Name the blood parasite species.
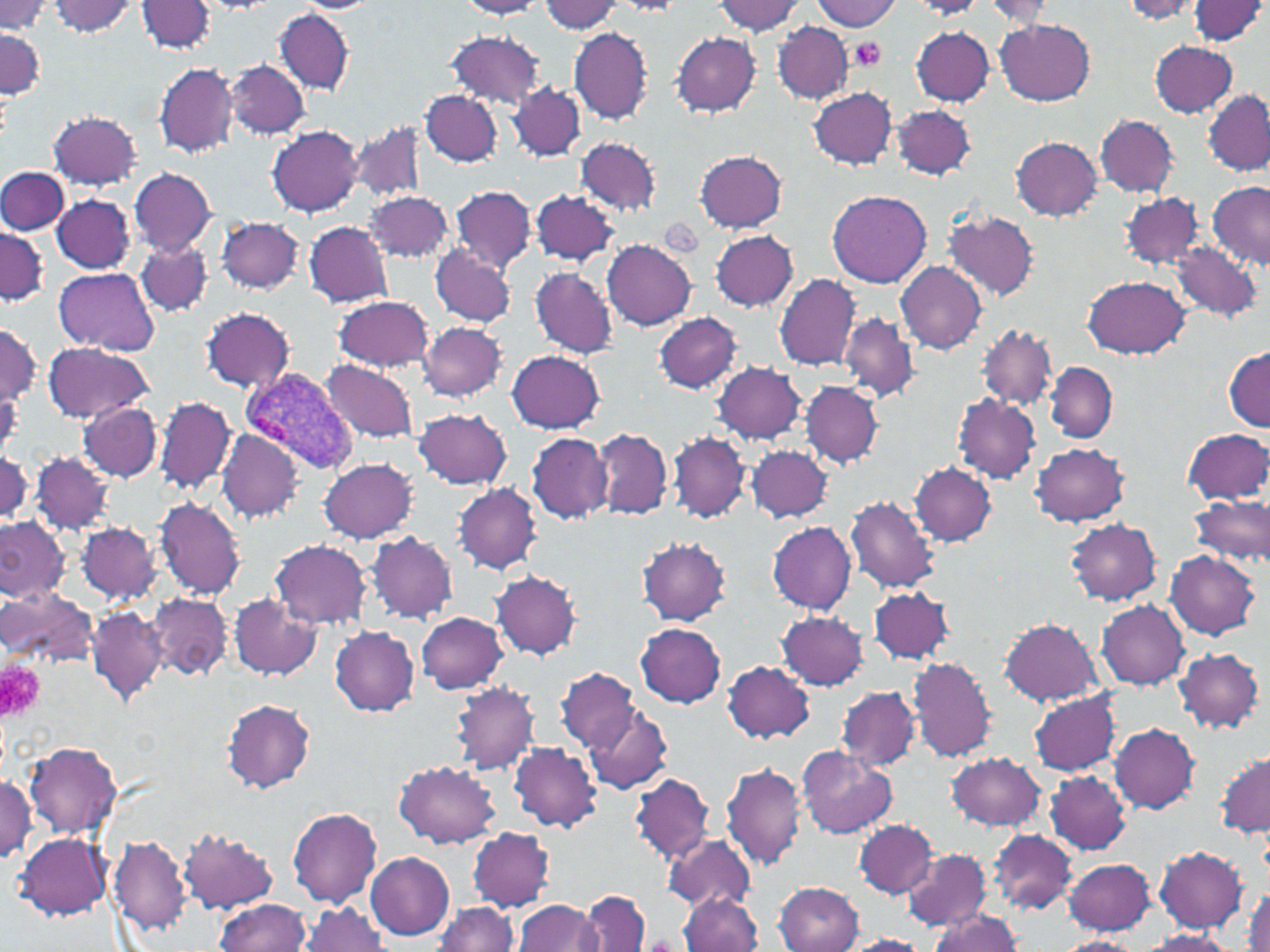
Plasmodium vivax.

Approximate bounding boxes as [x1, y1, x2, y2] in pixels. Plasmodium vivax-infected red blood cell locations: [240, 368, 359, 476]. Platelet locations: [849, 37, 887, 72], [0, 660, 43, 721]. Uninfected red blood cell locations: [50, 0, 138, 36], [456, 0, 545, 18], [715, 0, 805, 36], [1121, 0, 1202, 23], [1187, 0, 1268, 45], [138, 1, 215, 54], [294, 1, 376, 13], [540, 1, 624, 34], [814, 1, 900, 31], [911, 1, 981, 21], [982, 1, 1056, 27], [0, 2, 50, 34], [276, 8, 354, 95], [995, 19, 1095, 104], [773, 22, 853, 103], [568, 26, 653, 125], [911, 27, 995, 105], [1, 29, 43, 100], [445, 30, 545, 108], [672, 31, 762, 117], [1150, 40, 1237, 118], [224, 59, 309, 138], [153, 61, 240, 158], [509, 82, 586, 161], [809, 86, 896, 169], [1201, 89, 1270, 176], [419, 90, 501, 166], [890, 104, 975, 181], [47, 109, 143, 191], [1095, 114, 1180, 198], [349, 120, 429, 202], [267, 125, 363, 217], [575, 136, 660, 216], [1011, 137, 1103, 221], [694, 149, 788, 232], [0, 166, 69, 235], [128, 168, 217, 257], [1205, 183, 1270, 271], [1113, 184, 1211, 341], [450, 185, 534, 272], [827, 189, 932, 288], [529, 190, 618, 264], [366, 191, 453, 264], [1120, 191, 1205, 270], [51, 195, 136, 273], [944, 211, 1039, 302], [217, 217, 305, 295], [304, 220, 394, 307], [0, 226, 49, 306], [709, 229, 798, 311], [135, 238, 212, 315], [602, 240, 697, 331], [1168, 243, 1262, 322], [430, 245, 516, 326], [895, 260, 987, 354], [529, 266, 619, 359], [54, 267, 160, 355], [774, 274, 859, 372], [1081, 275, 1191, 357], [333, 294, 434, 373], [199, 306, 296, 392], [654, 312, 745, 392], [840, 312, 919, 402], [417, 322, 508, 402], [0, 324, 40, 405], [978, 324, 1056, 412], [41, 344, 154, 421], [1224, 347, 1270, 429], [506, 349, 606, 433], [320, 360, 419, 444], [1045, 361, 1117, 443], [712, 362, 807, 447], [800, 380, 883, 468], [156, 396, 235, 496], [952, 396, 1041, 483], [77, 401, 162, 482], [413, 408, 512, 490], [1182, 427, 1270, 506], [592, 428, 673, 520], [215, 429, 305, 522], [525, 431, 612, 524], [668, 431, 750, 523], [1029, 442, 1131, 527], [747, 445, 834, 523], [0, 448, 33, 521], [30, 452, 115, 534], [320, 458, 419, 543], [909, 461, 997, 546], [454, 483, 542, 575], [1191, 494, 1270, 571], [153, 496, 247, 600], [845, 496, 942, 594], [0, 516, 69, 602], [1066, 518, 1163, 607], [77, 521, 161, 602], [767, 521, 857, 614], [367, 532, 459, 623], [637, 536, 731, 625], [269, 538, 372, 630], [1165, 552, 1260, 639], [491, 570, 582, 660], [868, 586, 955, 665], [3, 588, 96, 665], [229, 593, 320, 679], [149, 594, 231, 679], [1097, 600, 1191, 689], [86, 605, 168, 706], [777, 610, 867, 689], [417, 612, 507, 694], [998, 617, 1104, 706], [635, 623, 726, 708], [330, 625, 420, 716], [1174, 647, 1264, 733], [908, 655, 998, 762], [723, 661, 816, 743], [558, 666, 640, 750], [451, 682, 540, 776], [836, 686, 920, 771], [1029, 691, 1122, 776], [222, 699, 315, 793], [584, 706, 672, 795], [1109, 722, 1200, 813], [25, 740, 122, 837], [508, 743, 602, 831], [796, 747, 896, 839], [945, 752, 1047, 832], [1215, 752, 1269, 837], [394, 760, 501, 848], [721, 761, 806, 872], [1046, 771, 1132, 855], [629, 772, 715, 864], [0, 775, 37, 863], [288, 807, 383, 907], [854, 819, 938, 898], [179, 826, 279, 915], [468, 826, 557, 912], [988, 829, 1076, 913], [661, 832, 756, 911], [16, 833, 111, 920], [108, 835, 192, 934], [1154, 846, 1247, 933], [901, 848, 990, 934], [366, 853, 455, 939], [1064, 857, 1157, 935], [775, 882, 863, 951], [1243, 886, 1270, 952], [581, 890, 651, 952], [679, 892, 764, 951], [214, 898, 310, 951], [514, 899, 605, 952], [301, 901, 388, 952], [432, 903, 517, 952], [932, 909, 1023, 951], [1140, 929, 1235, 951], [838, 934, 931, 952], [1057, 935, 1140, 952]. May-Grünwald-Giemsa-stained preparation. Single field of view. 1000x magnification. Image is 1270×952 pixels. Optical microscopy. Thin blood smear.